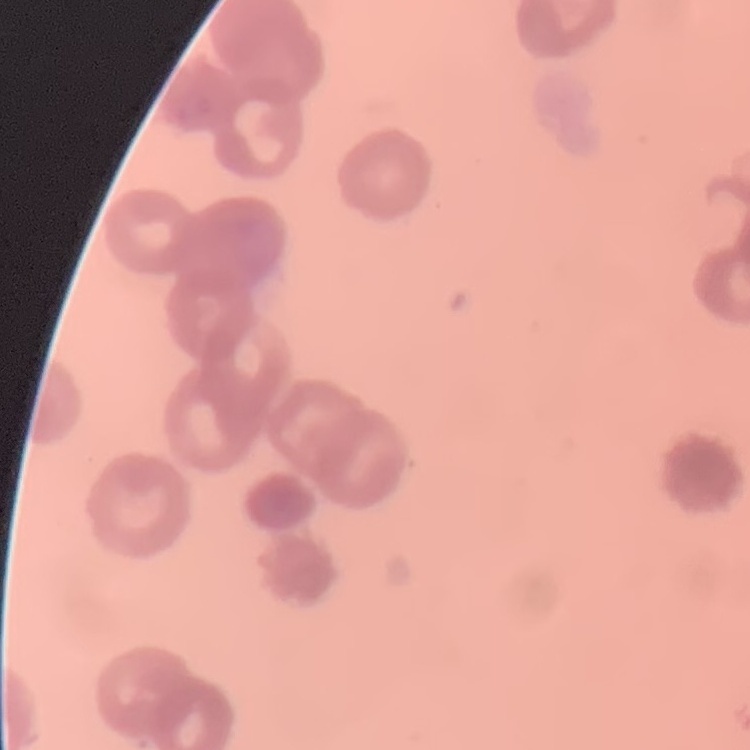
Summary:
  - Erythrocyte morphology: rouleaux formation
  - Stain: Field's or Giemsa
  - Image type: square crop of a larger photomicrograph
  - Preparation: thin peripheral smear